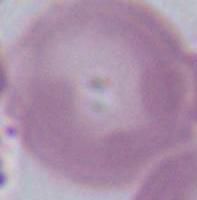

{
  "modality": "micrograph",
  "identification": "erythrocyte",
  "magnification": "1000x"
}